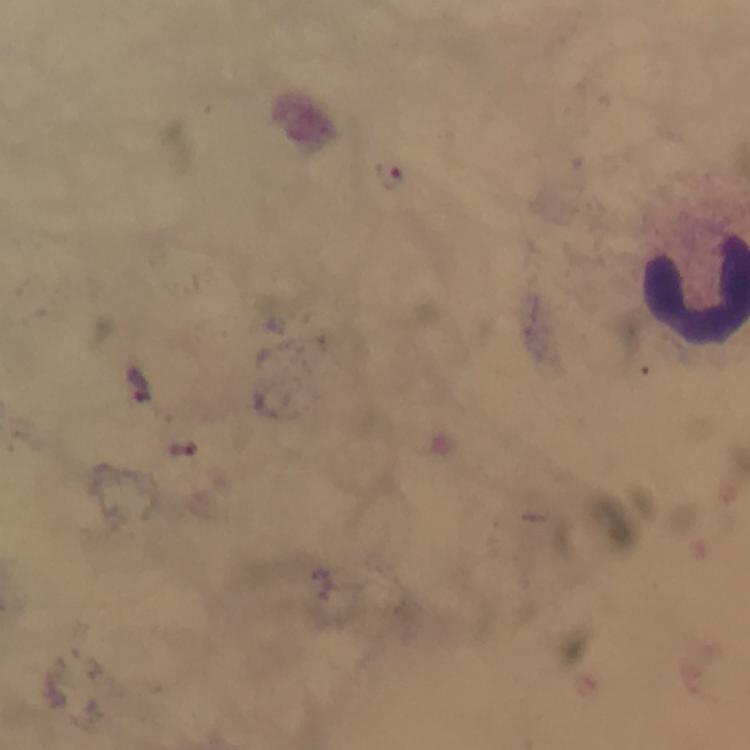

magnification = 100x
stain = Giemsa
image size = 750×750 pixels
malaria parasite locations = approximate centers as [x, y] in pixels: [390, 174], [139, 385], [182, 450]
cropped from = one field of view
immersion oil = applied
capture = smartphone camera through the microscope
context = from a diagnostic examination for malaria
preparation = thick blood smear